Locate every Plasmodium falciparum-infected red blood cell.
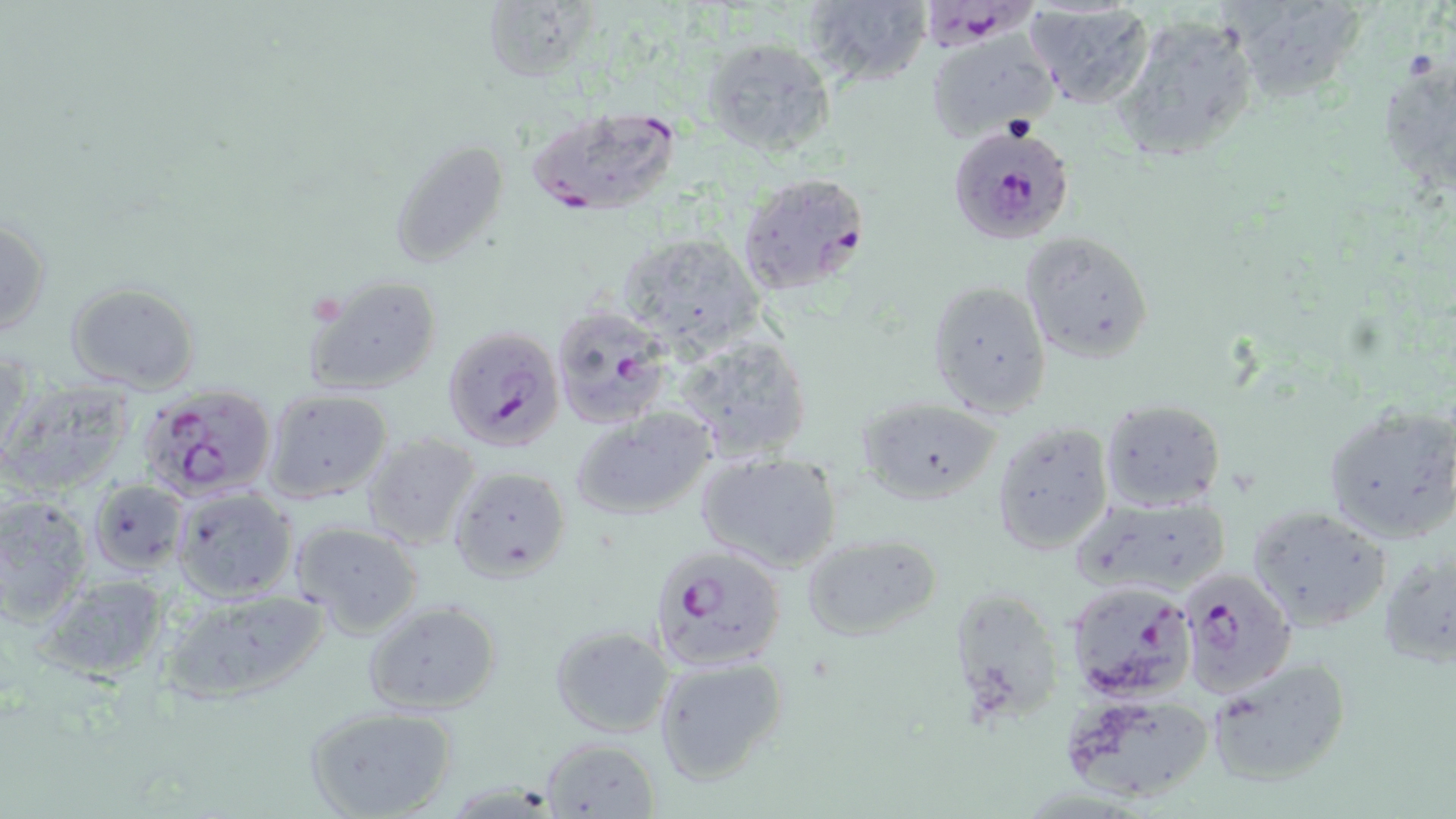

Approximate bounding boxes as named x1/y1/x2/y2 corners in pixels.
Plasmodium falciparum-infected red blood cells: (x1=922, y1=2, x2=1044, y2=63), (x1=523, y1=106, x2=686, y2=218), (x1=947, y1=125, x2=1074, y2=244), (x1=736, y1=172, x2=873, y2=299), (x1=549, y1=305, x2=673, y2=429), (x1=440, y1=325, x2=565, y2=453), (x1=136, y1=383, x2=278, y2=501), (x1=647, y1=543, x2=786, y2=671), (x1=1180, y1=569, x2=1296, y2=699), (x1=1062, y1=578, x2=1197, y2=702).

slide-level diagnosis = Plasmodium falciparum
field of view = single
modality = optical microscopy
preparation = thin blood smear
magnification = 1000x
image size = 1456×819 pixels
stain = May-Grünwald-Giemsa
uninfected red blood cell locations = approximate bounding boxes as named x1/y1/x2/y2 corners in pixels: (x1=480, y1=0, x2=593, y2=83), (x1=800, y1=0, x2=932, y2=93), (x1=1226, y1=1, x2=1369, y2=106), (x1=1024, y1=2, x2=1157, y2=110), (x1=1109, y1=14, x2=1261, y2=167), (x1=925, y1=32, x2=1057, y2=144), (x1=700, y1=34, x2=838, y2=157), (x1=1377, y1=59, x2=1454, y2=189), (x1=388, y1=136, x2=514, y2=269), (x1=0, y1=215, x2=51, y2=343), (x1=613, y1=230, x2=768, y2=353), (x1=1019, y1=232, x2=1155, y2=362), (x1=302, y1=273, x2=445, y2=396), (x1=927, y1=280, x2=1054, y2=416), (x1=64, y1=281, x2=201, y2=394), (x1=675, y1=333, x2=814, y2=463), (x1=1, y1=379, x2=137, y2=497), (x1=261, y1=388, x2=395, y2=505), (x1=857, y1=397, x2=1002, y2=504), (x1=1099, y1=398, x2=1226, y2=513), (x1=1322, y1=404, x2=1456, y2=542), (x1=569, y1=407, x2=716, y2=523), (x1=993, y1=420, x2=1113, y2=554), (x1=360, y1=432, x2=482, y2=552), (x1=696, y1=451, x2=844, y2=574), (x1=446, y1=465, x2=573, y2=582), (x1=89, y1=479, x2=188, y2=572), (x1=172, y1=487, x2=298, y2=602), (x1=1071, y1=493, x2=1233, y2=599), (x1=0, y1=494, x2=91, y2=626), (x1=1246, y1=504, x2=1394, y2=633), (x1=289, y1=521, x2=424, y2=638), (x1=801, y1=534, x2=941, y2=640), (x1=1379, y1=548, x2=1455, y2=664), (x1=32, y1=576, x2=173, y2=682), (x1=947, y1=585, x2=1066, y2=727), (x1=154, y1=588, x2=334, y2=708), (x1=363, y1=600, x2=501, y2=714), (x1=549, y1=625, x2=673, y2=738), (x1=651, y1=654, x2=789, y2=786), (x1=1203, y1=657, x2=1352, y2=790), (x1=1059, y1=691, x2=1217, y2=806), (x1=306, y1=708, x2=454, y2=819), (x1=540, y1=737, x2=660, y2=817)